Classify this cell by malaria status.
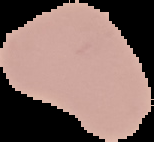
It is uninfected.

Summary:
  - Image type: cell region segmented out of the field of view; surrounding area masked to black
  - Preparation: thin blood film
  - Image size: 154×142 pixels